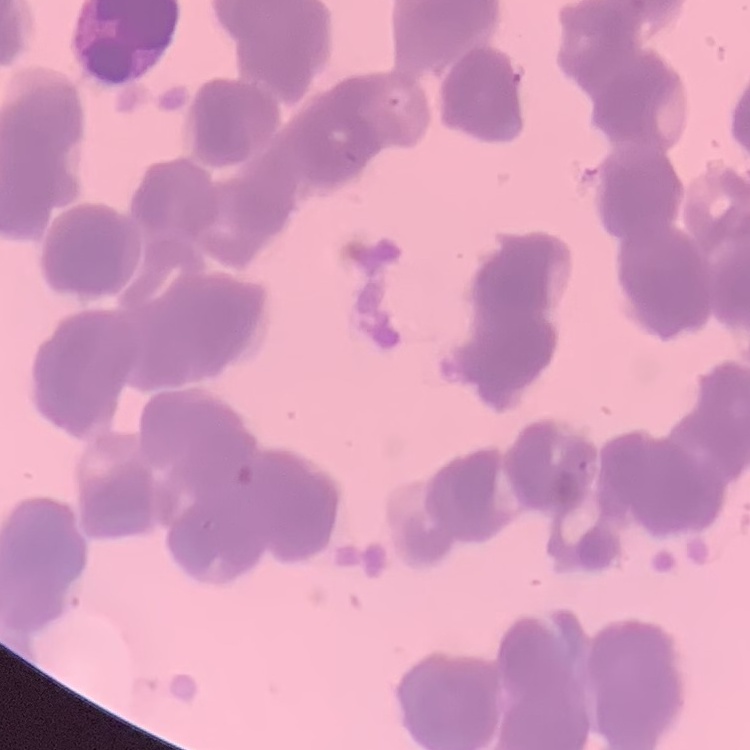
The erythrocytes show rouleaux formation. Thin peripheral smear. Field's or Giemsa stain. Square crop of a larger photomicrograph.